Identify the parasite.
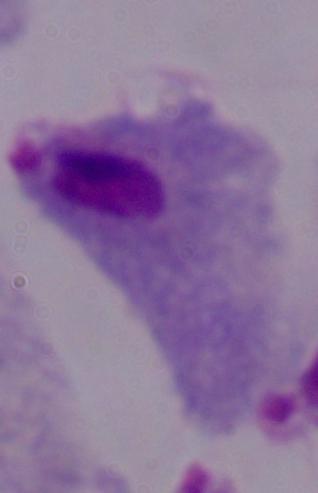

This is a trichomonad.

1000x magnification. Micrograph.